Classify this cell by malaria status.
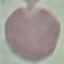

Uninfected.

{
  "stain": "Giemsa",
  "capture": "smartphone through the microscope eyepiece",
  "preparation": "thin blood film",
  "image_type": "cell patch, automatically extracted from a larger field of view and resized to 64 × 64 pixels"
}